Identify the parasite.
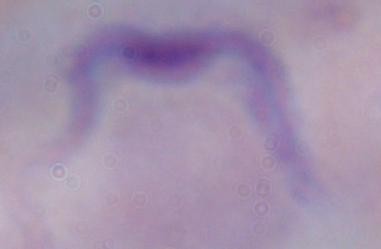

This is a trypanosome.

modality = micrograph
magnification = 1000x